Locate every Plasmodium parasite.
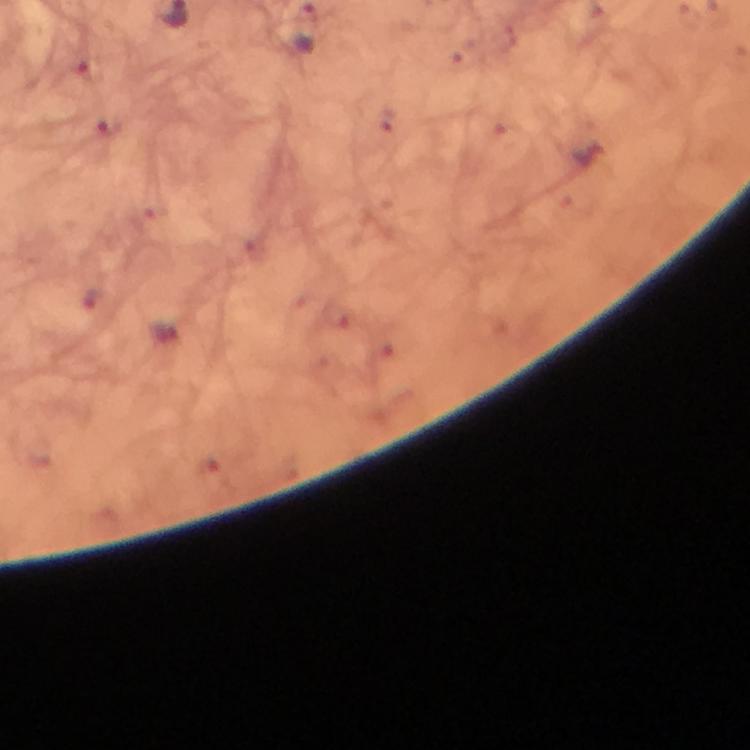

Approximate centers as (x, y) in pixels.
Plasmodium parasites: (109, 127), (164, 332).

{
  "stain": "Giemsa",
  "capture": "smartphone mounted on the microscope",
  "cropped_from": "a single field of view",
  "immersion_oil": "applied",
  "preparation": "thick blood smear",
  "magnification": "100x",
  "image_size": "750×750 pixels",
  "context": "from a diagnostic examination for malaria"
}